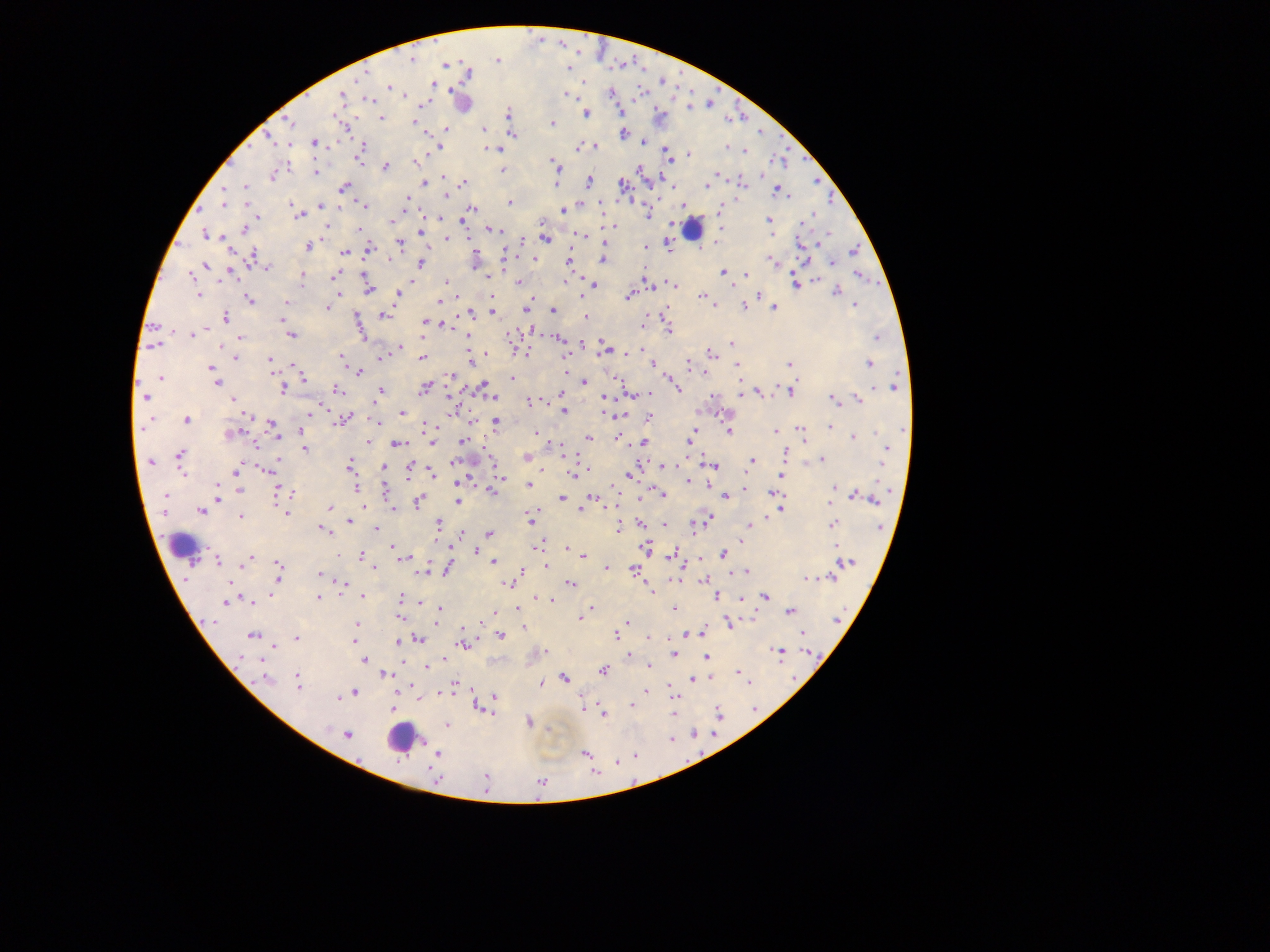
Approximate centers as (x, y) in pixels. Malaria parasite locations: (411, 60), (497, 60), (566, 67), (360, 77), (389, 87), (611, 94), (567, 95), (341, 96), (371, 99), (689, 107), (506, 113), (586, 114), (381, 118), (414, 120), (290, 123), (552, 123), (446, 129), (483, 129), (512, 134), (623, 134), (268, 138), (643, 141), (314, 142), (288, 145), (578, 146), (597, 146), (441, 147), (726, 147), (491, 149), (361, 150), (743, 150), (689, 154), (360, 158), (669, 159), (553, 161), (417, 162), (385, 166), (502, 169), (315, 173), (717, 173), (273, 175), (443, 178), (589, 182), (424, 183), (462, 183), (556, 183), (743, 184), (622, 185), (707, 185), (245, 187), (344, 187), (224, 188), (776, 191), (446, 195), (407, 199), (509, 203), (225, 205), (321, 206), (364, 206), (292, 207), (473, 209), (563, 210), (719, 210), (648, 214), (300, 215), (810, 216), (257, 217), (438, 218), (769, 220), (805, 221), (391, 222), (614, 226), (244, 229), (359, 229), (492, 230), (420, 232), (204, 234), (580, 235), (447, 238), (544, 238), (400, 243), (800, 243), (669, 245), (307, 247), (369, 248), (646, 248), (230, 250), (853, 251), (345, 252), (251, 256), (534, 258), (602, 259), (390, 260), (569, 260), (772, 261), (832, 262), (420, 263), (205, 264), (266, 268), (231, 271), (723, 272), (746, 274), (365, 275), (489, 275), (858, 275), (191, 276), (333, 276), (303, 278), (815, 281), (446, 282), (519, 283), (301, 284), (673, 284), (593, 285), (795, 285), (651, 286), (367, 289), (835, 292), (198, 294), (337, 294), (397, 295), (629, 296), (703, 296), (491, 297), (759, 297), (249, 300), (438, 301), (286, 303), (715, 305), (856, 305), (528, 306), (327, 307), (743, 307), (525, 308), (774, 308), (553, 310), (472, 313), (492, 313), (664, 313), (383, 315), (226, 317), (585, 318), (282, 319), (424, 321), (430, 322), (642, 324), (442, 326), (172, 331), (669, 331), (194, 335), (290, 335), (878, 337), (241, 339), (560, 340), (732, 344), (155, 345), (221, 347), (399, 347), (603, 351), (525, 352), (629, 353), (711, 353), (566, 356), (236, 357), (470, 357), (380, 358), (422, 358), (270, 359), (342, 359), (789, 364), (869, 364), (293, 365), (653, 365), (688, 365), (738, 365), (211, 369), (359, 372), (703, 372), (450, 375), (160, 378), (304, 379), (513, 379), (615, 379), (584, 382), (218, 383), (896, 384), (483, 386), (424, 388), (283, 389), (337, 389), (678, 389), (380, 391), (789, 392), (741, 393), (759, 393), (489, 394), (632, 394), (561, 395), (146, 397), (233, 398), (494, 398), (833, 399), (859, 399), (529, 402), (563, 410), (402, 412), (310, 413), (620, 415), (649, 418), (186, 420), (343, 421), (375, 421), (496, 421), (473, 423), (271, 424), (426, 427), (829, 427), (801, 429), (694, 430), (301, 431), (729, 432), (775, 432), (535, 433), (232, 434), (803, 436), (854, 437), (588, 438), (617, 438), (368, 442), (462, 442), (644, 442), (688, 442), (432, 443), (397, 444), (560, 444), (305, 449), (886, 450), (785, 453), (180, 456), (527, 458), (821, 459), (752, 460), (151, 462), (453, 463), (663, 466), (715, 466), (349, 467), (384, 467), (266, 469), (236, 470), (588, 470), (409, 473), (431, 474), (573, 475), (629, 475), (500, 476), (781, 477), (688, 481), (458, 482), (529, 485), (355, 488), (744, 488), (834, 488), (217, 490), (239, 490), (385, 491), (289, 492), (493, 492), (773, 492), (277, 493), (165, 495), (663, 495), (858, 496), (727, 497), (562, 498), (592, 498), (217, 499), (872, 499), (419, 501), (457, 501), (831, 503), (329, 507), (393, 509), (580, 509), (781, 510), (201, 511), (287, 513), (532, 515), (240, 517), (530, 519), (709, 519), (349, 521), (439, 523), (640, 523), (751, 524), (833, 524), (664, 525), (879, 527), (376, 528), (324, 529), (617, 529), (463, 533), (490, 534), (392, 546), (537, 547), (645, 548), (567, 549), (476, 552), (361, 555), (673, 555), (724, 555), (584, 556), (250, 558), (404, 559), (217, 561), (494, 562), (846, 563), (546, 566), (375, 567), (278, 569), (607, 569), (634, 569), (447, 570), (521, 571), (422, 572), (746, 572), (320, 574), (831, 576), (807, 578), (704, 580), (345, 582), (508, 584), (570, 584), (651, 591), (271, 594), (362, 596), (717, 596), (765, 596), (319, 597), (400, 597), (539, 599), (550, 601), (226, 602), (251, 602), (420, 602), (440, 608), (590, 608), (518, 609), (674, 609), (791, 611), (495, 612), (587, 612), (399, 618), (580, 618), (357, 622), (436, 622), (627, 623), (729, 623), (524, 628), (701, 633), (803, 633), (689, 634), (501, 635), (251, 636), (616, 636), (296, 638), (650, 638), (418, 639), (353, 641), (399, 642), (462, 644), (274, 648), (545, 651), (778, 652), (673, 654), (629, 655), (242, 656), (706, 656), (261, 660), (364, 660), (443, 661), (648, 666), (427, 667), (603, 671), (738, 672), (385, 674), (565, 678), (693, 679), (266, 680), (297, 682), (748, 683), (456, 684), (542, 685), (646, 691), (354, 693), (440, 693), (495, 697), (338, 698), (631, 705), (479, 708), (391, 709), (673, 713), (603, 715), (528, 721), (446, 725), (347, 734), (425, 744), (585, 753), (436, 755), (435, 777), (486, 779). Leukocyte locations: (459, 99), (692, 229), (182, 545), (398, 738). Thick blood film. Photographed through a microscope with a mobile-phone camera. Collected in Ghana. One field of view. Image is 1270×952 pixels.